Classify this cell by malaria status.
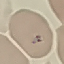

Parasitized.

Giemsa stain. Cell patch, automatically extracted from a larger field of view and resized to 64 × 64 pixels. Photographed with a smartphone camera at the microscope eyepiece. Thin blood smear.